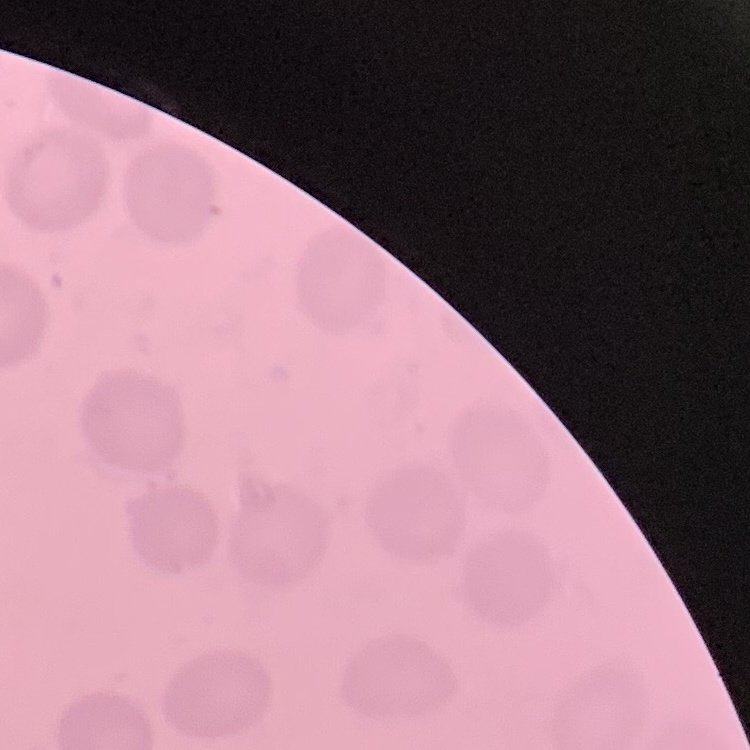

Summary:
  - Erythrocyte morphology: no rouleaux formation
  - Preparation: thin blood smear
  - Stain: Field's or Giemsa
  - Image type: square crop of a larger photomicrograph